Classify this cell by malaria status.
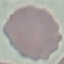

Uninfected.

Summary:
  - Preparation: thin blood film
  - Capture: smartphone camera at the microscope eyepiece
  - Stain: Giemsa
  - Image type: automatically extracted cell patch, resized to 64 × 64 pixels